Describe the morphology of the red blood cells.
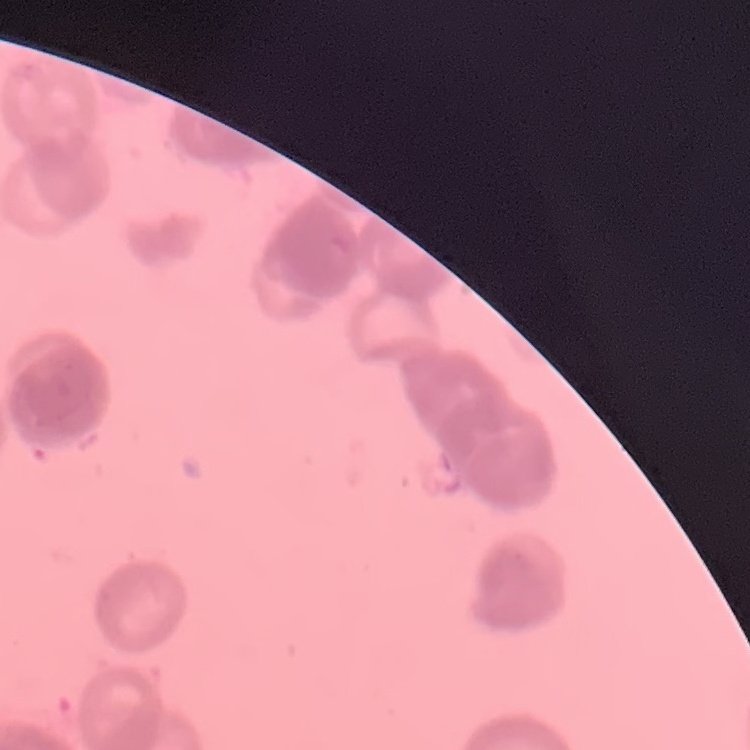
They show rouleaux formation.

image type = square crop of a larger photomicrograph
preparation = thin peripheral smear
stain = Field's or Giemsa